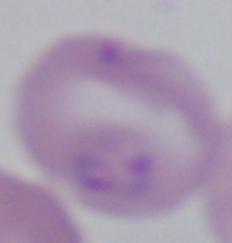

Summary:
  - Modality: micrograph
  - Magnification: 1000x
  - Identification: Babesia